Report the malaria status of this cell.
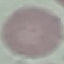

It is uninfected.

Summary:
  - Preparation: thin blood smear
  - Stain: Giemsa
  - Capture: smartphone through the microscope eyepiece
  - Image type: automatically extracted cell patch, resized to 64 × 64 pixels